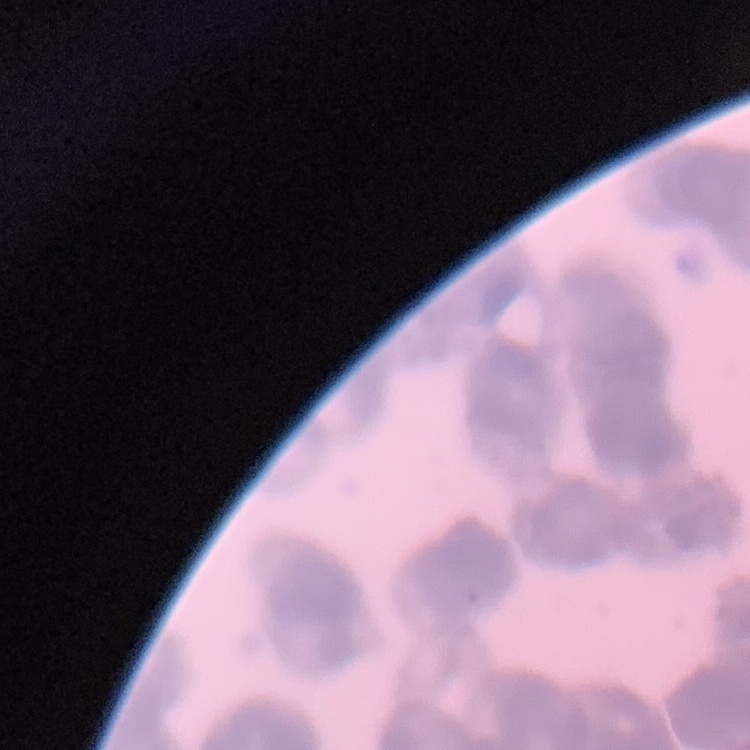

red_blood_cell_morphology: rouleaux formation
image_type: one tile cut from a larger photomicrograph
preparation: thin blood film
stain: Field's or Giemsa